Identify the parasite.
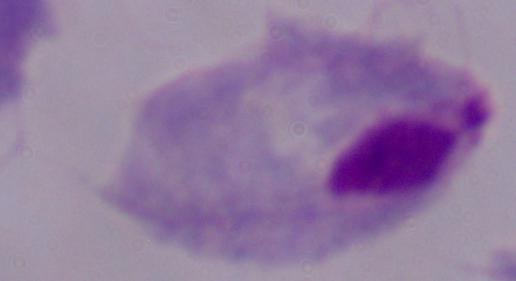
This is a trichomonad.

Photomicrograph. 1000x magnification.